Assess this cell for malaria.
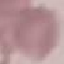
It is uninfected.

Summary:
  - Stain: Giemsa
  - Preparation: thin blood smear
  - Capture: smartphone camera at the microscope eyepiece
  - Image type: cell patch, automatically extracted from a larger field of view and resized to 64 × 64 pixels